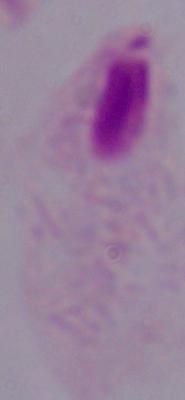
Summary:
  - Identification: trichomonad
  - Magnification: 1000x
  - Modality: photomicrograph